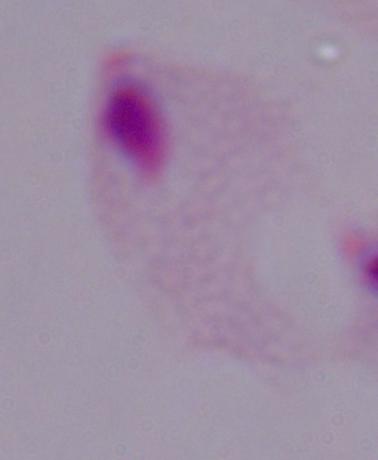 Captured at 1000x magnification. Photomicrograph. A trichomonad is shown.